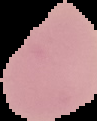
Summary:
  - Result: no Plasmodium parasites detected
  - Image type: segmented cell region on a black background
  - Image size: 97×121 pixels
  - Preparation: thin blood smear